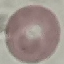

Summary:
  - Malaria status: uninfected
  - Stain: Giemsa
  - Capture: smartphone camera at the microscope eyepiece
  - Preparation: thin blood smear
  - Image type: cell patch, automatically extracted from a larger field of view and resized to 64 × 64 pixels